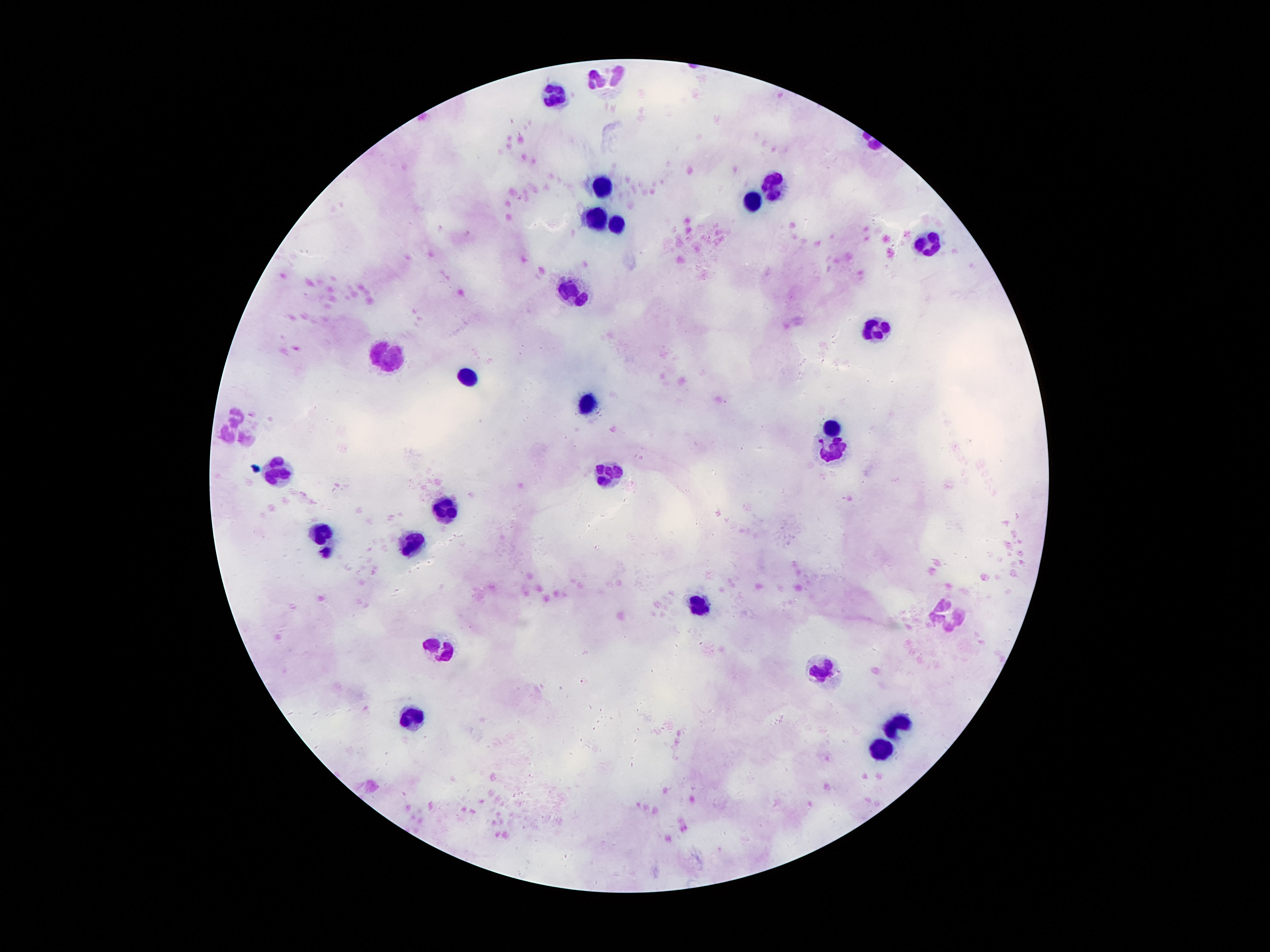

Approximate centers as {x, y} in pixels.
Summary:
  - Leukocyte locations: {605, 78}, {557, 95}, {773, 183}, {601, 189}, {752, 204}, {597, 218}, {616, 227}, {925, 244}, {572, 293}, {874, 333}, {387, 357}, {467, 376}, {589, 405}, {236, 425}, {830, 427}, {832, 454}, {278, 471}, {608, 473}, {444, 509}, {318, 532}, {414, 539}, {700, 606}, {948, 613}, {440, 650}, {821, 669}, {412, 720}, {893, 726}, {880, 751}
  - Magnification: 100x
  - Field of view: one from this slide
  - Preparation: thick blood film
  - Patient malaria status: not infected
  - Capture: smartphone camera through the microscope eyepiece
  - Stain: Giemsa
  - Image size: 1270×952 pixels